Give the extent of all Plasmodium falciparum-infected red blood cells.
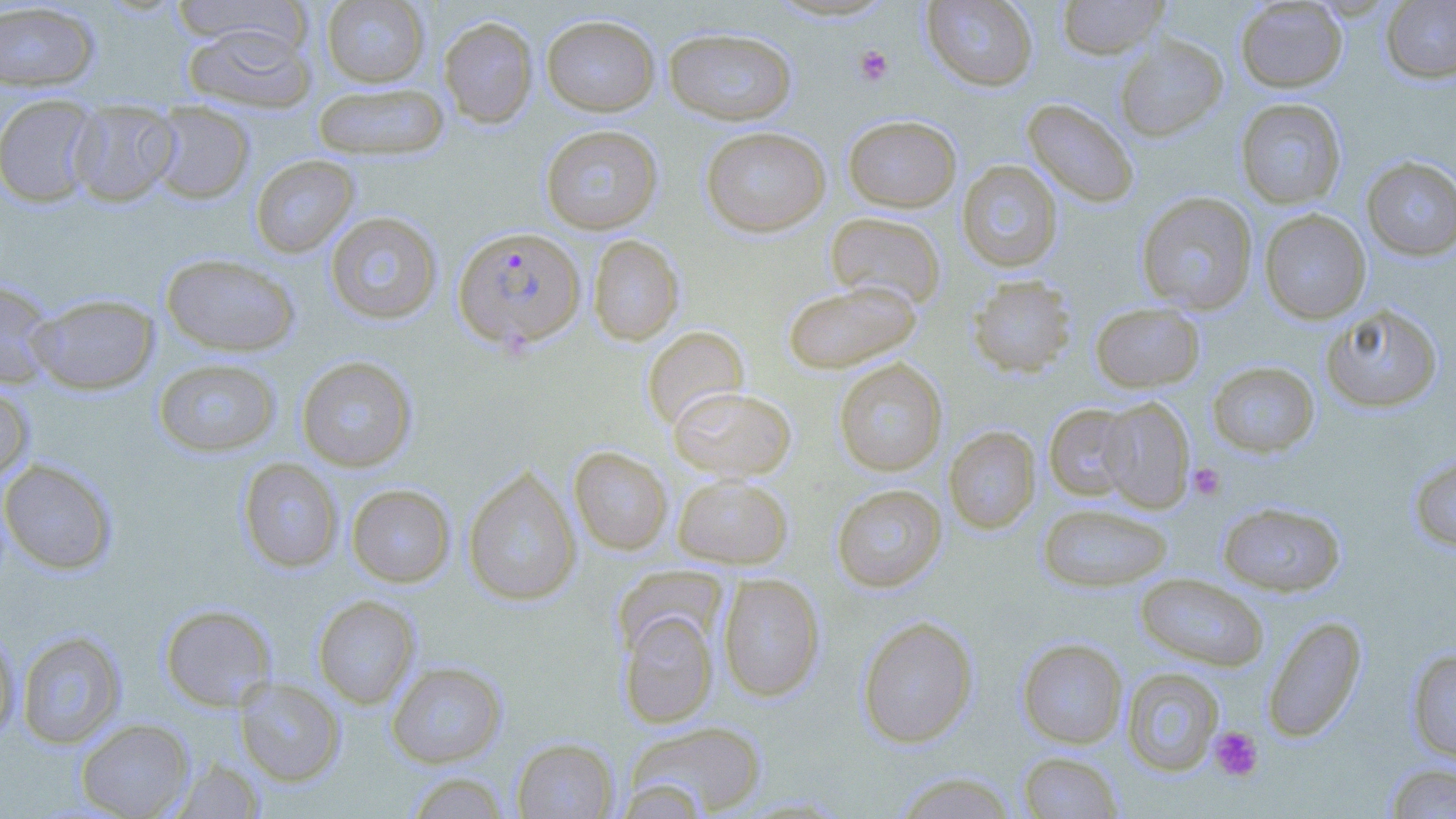

Approximate bounding boxes as [x1, y1, x2, y2] in pixels.
Plasmodium falciparum-infected red blood cells: [453, 226, 586, 352].

{
  "slide_level_diagnosis": "Plasmodium falciparum",
  "platelet_locations": "approximate bounding boxes as [x1, y1, x2, y2] in pixels: [854, 45, 893, 85], [1188, 462, 1226, 501], [1209, 725, 1264, 782]",
  "image_size": "1456×819 pixels",
  "uninfected_red_blood_cell_locations": "approximate bounding boxes as [x1, y1, x2, y2] in pixels: [169, 0, 314, 55], [321, 0, 431, 87], [920, 0, 1039, 91], [1055, 0, 1170, 60], [1235, 0, 1348, 92], [1381, 1, 1456, 83], [0, 2, 101, 92], [541, 14, 660, 116], [438, 15, 538, 128], [182, 23, 316, 113], [663, 27, 798, 125], [1114, 35, 1228, 141], [312, 82, 449, 161], [0, 93, 102, 208], [1022, 98, 1139, 208], [1235, 98, 1347, 209], [68, 99, 180, 207], [147, 102, 255, 205], [843, 115, 962, 212], [540, 124, 663, 235], [700, 126, 830, 237], [251, 154, 359, 257], [1361, 156, 1456, 261], [956, 160, 1063, 272], [1137, 191, 1258, 315], [1259, 209, 1371, 324], [324, 211, 443, 325], [825, 212, 946, 310], [588, 235, 685, 345], [161, 252, 300, 356], [967, 275, 1077, 378], [0, 278, 58, 389], [782, 280, 922, 374], [29, 293, 158, 395], [1089, 302, 1205, 392], [1320, 303, 1443, 413], [641, 325, 749, 431], [296, 355, 418, 472], [153, 358, 281, 457], [833, 358, 948, 476], [1207, 360, 1320, 457], [0, 382, 35, 484], [668, 386, 796, 480], [1098, 397, 1195, 513], [1044, 404, 1139, 501], [944, 426, 1041, 533], [569, 446, 672, 555], [1409, 451, 1456, 554], [238, 457, 343, 573], [0, 458, 118, 574], [463, 465, 581, 606], [672, 474, 793, 569], [831, 483, 946, 592], [346, 484, 455, 587], [1217, 501, 1346, 596], [1037, 502, 1172, 592], [717, 573, 825, 701], [1135, 573, 1269, 671], [313, 594, 420, 709], [160, 604, 277, 711], [617, 610, 718, 728], [1261, 614, 1367, 742], [857, 615, 978, 748], [0, 626, 21, 743], [16, 630, 126, 749], [1016, 638, 1127, 749], [1407, 647, 1456, 763], [387, 661, 507, 767], [1121, 667, 1224, 776], [235, 677, 345, 785], [75, 718, 195, 818], [625, 720, 767, 816], [512, 737, 619, 818], [1018, 751, 1123, 818], [169, 757, 266, 818], [1383, 762, 1456, 818], [403, 771, 512, 818], [891, 771, 1021, 818], [613, 778, 711, 818]",
  "stain": "May-Grünwald-Giemsa",
  "preparation": "thin blood film",
  "modality": "optical microscopy",
  "magnification": "1000x",
  "field_of_view": "single"
}